State which parasite is depicted.
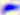
This is Toxoplasma gondii.

magnification = 400x
modality = photomicrograph